Assess this cell for malaria.
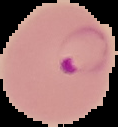
Parasitized.

Summary:
  - Image type: segmented cell region on a black background
  - Image size: 118×127 pixels
  - Preparation: thin blood film